Comment on the morphology of the erythrocytes.
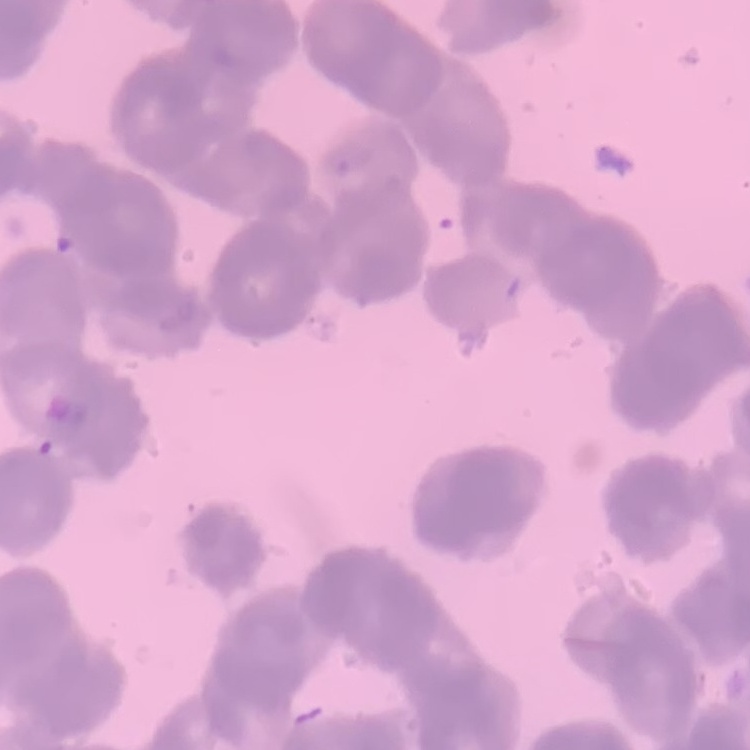
Rouleaux formation.

preparation = thin blood film
image type = square crop of a larger photomicrograph
stain = Field's or Giemsa